Assess the morphology of the erythrocytes.
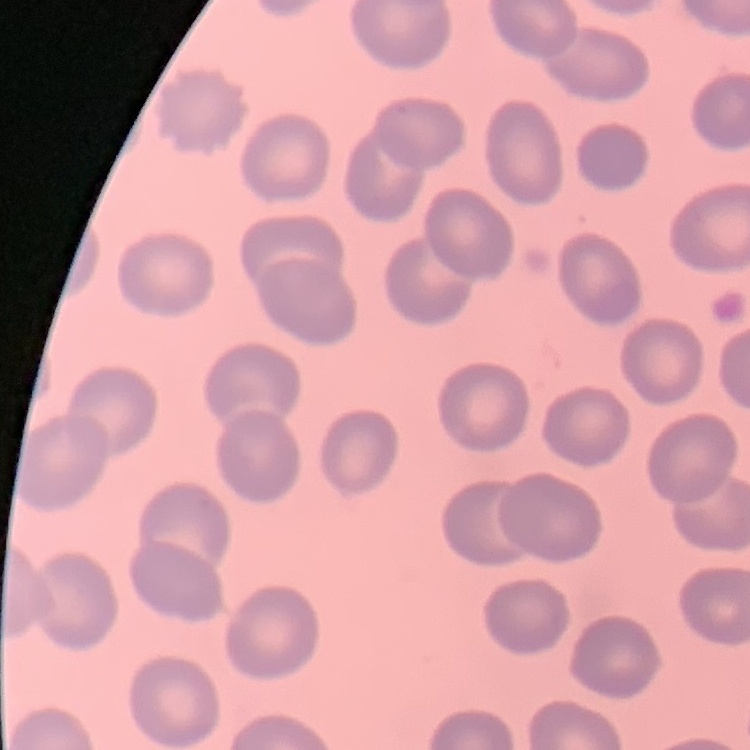

They show no rouleaux formation.

Summary:
  - Stain: Field's or Giemsa
  - Preparation: thin blood smear
  - Image type: square crop of a larger photomicrograph